Evaluate for malaria.
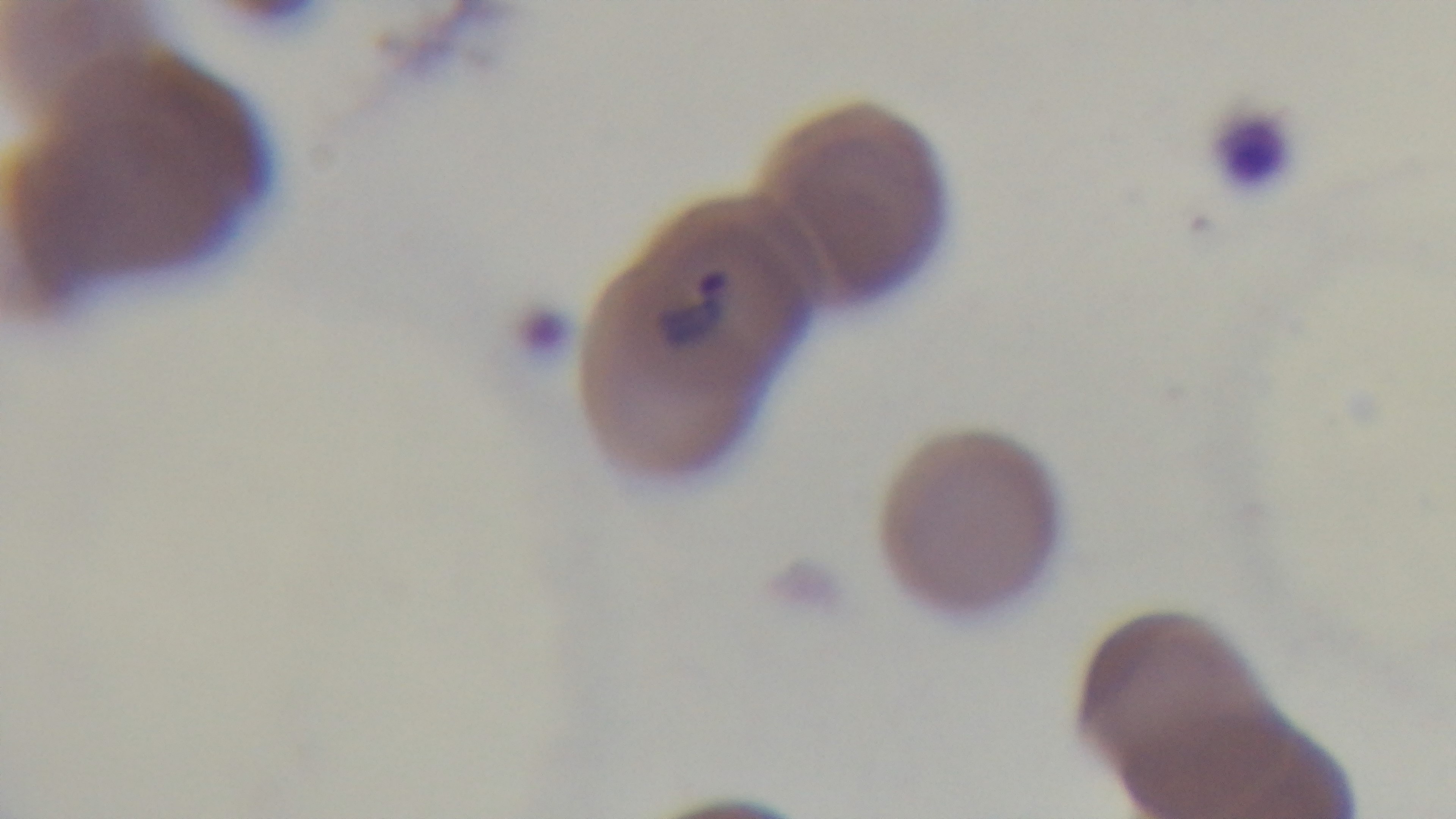
Positive.

Summary:
  - Stain: Giemsa
  - Modality: light microscopy
  - Objective: 100x oil immersion
  - Field of view: single
  - Preparation: thin smear
  - Capture: mounted 4K digital camera